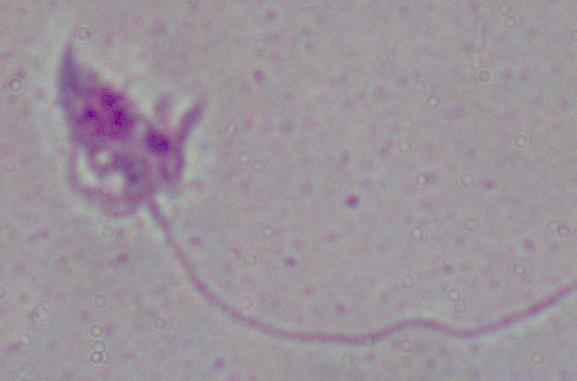 Captured at 1000x magnification. A Leishmania parasite is seen. Micrograph.